Outline each Trypanosoma brucei.
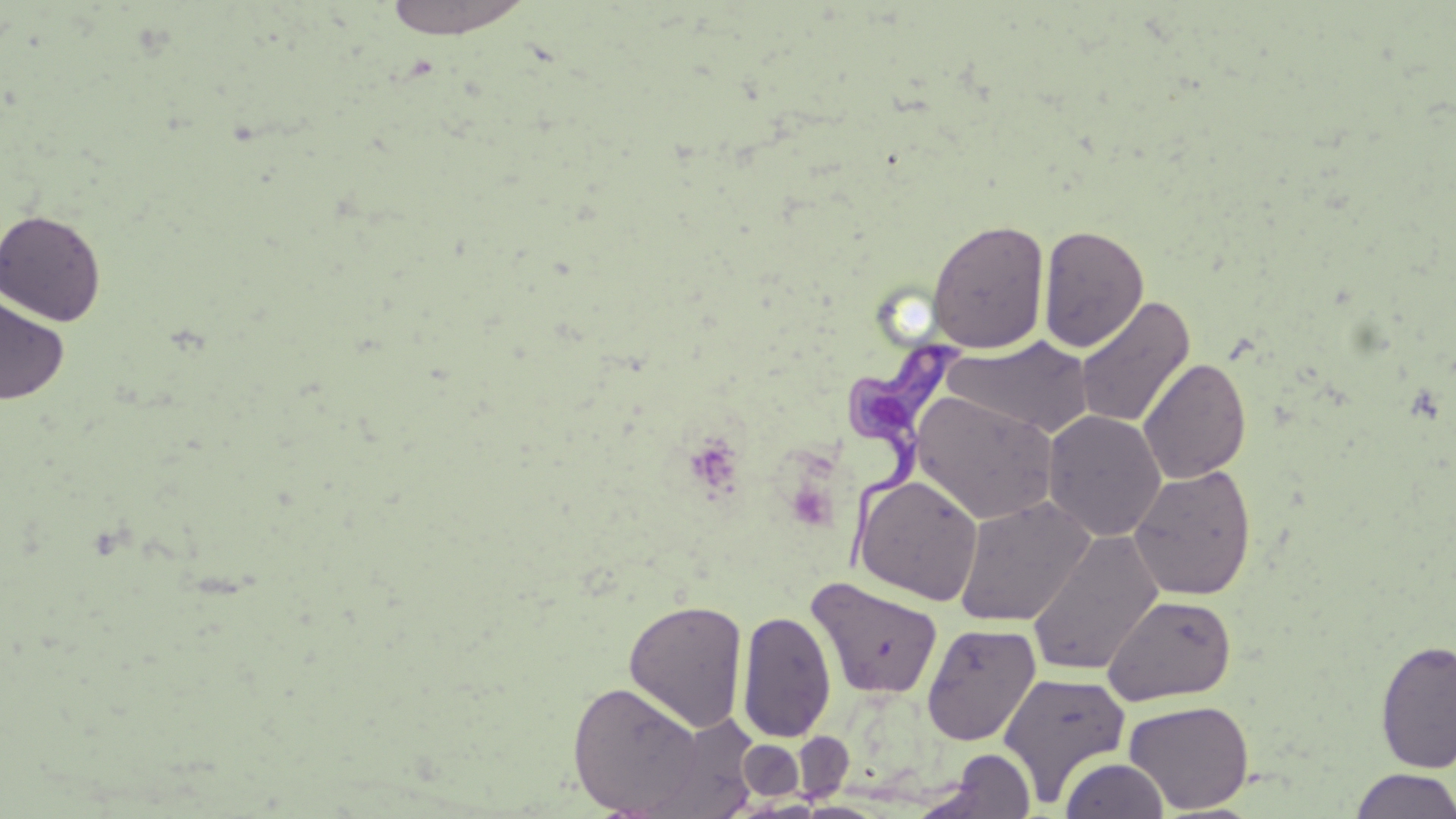
Approximate bounding boxes as [x1, y1, x2, y2] in pixels.
Trypanosoma brucei: [841, 339, 966, 579].

Uninfected red blood cell locations: [381, 0, 537, 40], [0, 208, 107, 326], [927, 219, 1050, 353], [1038, 224, 1149, 352], [0, 294, 69, 405], [1075, 295, 1196, 430], [943, 337, 1095, 441], [1138, 357, 1252, 485], [910, 390, 1060, 525], [1042, 410, 1167, 542], [1129, 464, 1256, 601], [853, 474, 984, 605], [953, 496, 1095, 626], [1026, 530, 1164, 677], [807, 576, 944, 700], [1102, 594, 1237, 706], [623, 598, 748, 732], [737, 609, 837, 744], [922, 623, 1040, 745], [1375, 639, 1456, 774], [998, 671, 1131, 805], [568, 680, 706, 815], [1124, 699, 1254, 814], [640, 714, 761, 817], [791, 731, 853, 803], [738, 739, 804, 801], [928, 748, 1037, 818], [1060, 757, 1170, 819], [1349, 769, 1456, 819]. Slide-level diagnosis: Trypanosoma brucei. Thin blood smear. One field of a larger specimen. Light microscopy. May-Grünwald-Giemsa stain. Captured at 1000x magnification. Image is 1456×819 pixels.